Classify the preparation.
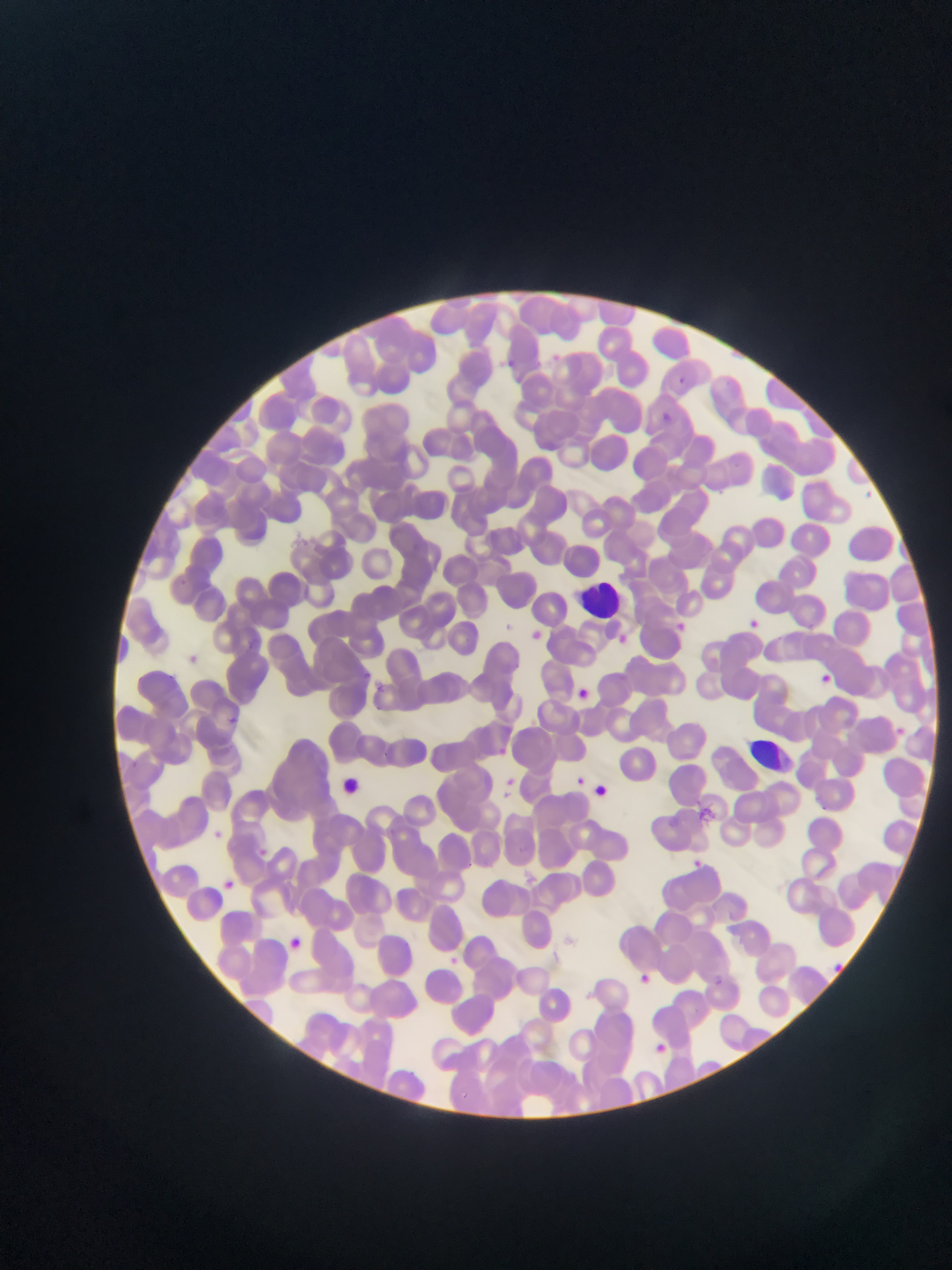
This is a thin smear.

Approximate bounding boxes as (left, top, right, bottom) in pixels. Leukocyte locations: (583, 575, 621, 613), (746, 734, 799, 777). Plasmodium parasite locations: (547, 350, 564, 366), (499, 356, 520, 374), (673, 375, 687, 389), (654, 411, 674, 430), (867, 489, 873, 498), (745, 616, 761, 632), (672, 620, 688, 634), (525, 627, 545, 646), (614, 633, 631, 649), (815, 671, 836, 689), (369, 680, 389, 698), (571, 685, 593, 705), (229, 717, 241, 728), (893, 725, 908, 739), (491, 743, 510, 761), (497, 774, 519, 798), (572, 774, 588, 789), (566, 775, 598, 793), (206, 827, 226, 845), (253, 844, 272, 862), (688, 857, 705, 872), (219, 876, 238, 894), (281, 934, 308, 957), (443, 953, 461, 970), (832, 959, 847, 973), (635, 970, 654, 988), (714, 971, 725, 989), (651, 1040, 669, 1057). One field of view. Image is 952×1270 pixels. Mobile-phone photograph taken through the microscope. Sample from Ghana.